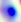
Summary:
  - Modality: photomicrograph
  - Identification: Toxoplasma gondii
  - Magnification: 400x